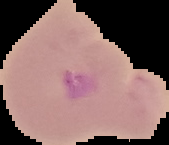
malaria status = parasitized
image type = segmented cell region with the area outside set to black
preparation = thin blood film
image size = 169×145 pixels